Classify this cell by malaria status.
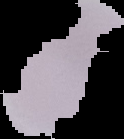
Uninfected.

Summary:
  - Preparation: thin blood smear
  - Image size: 124×139 pixels
  - Image type: segmented cell region on a black background